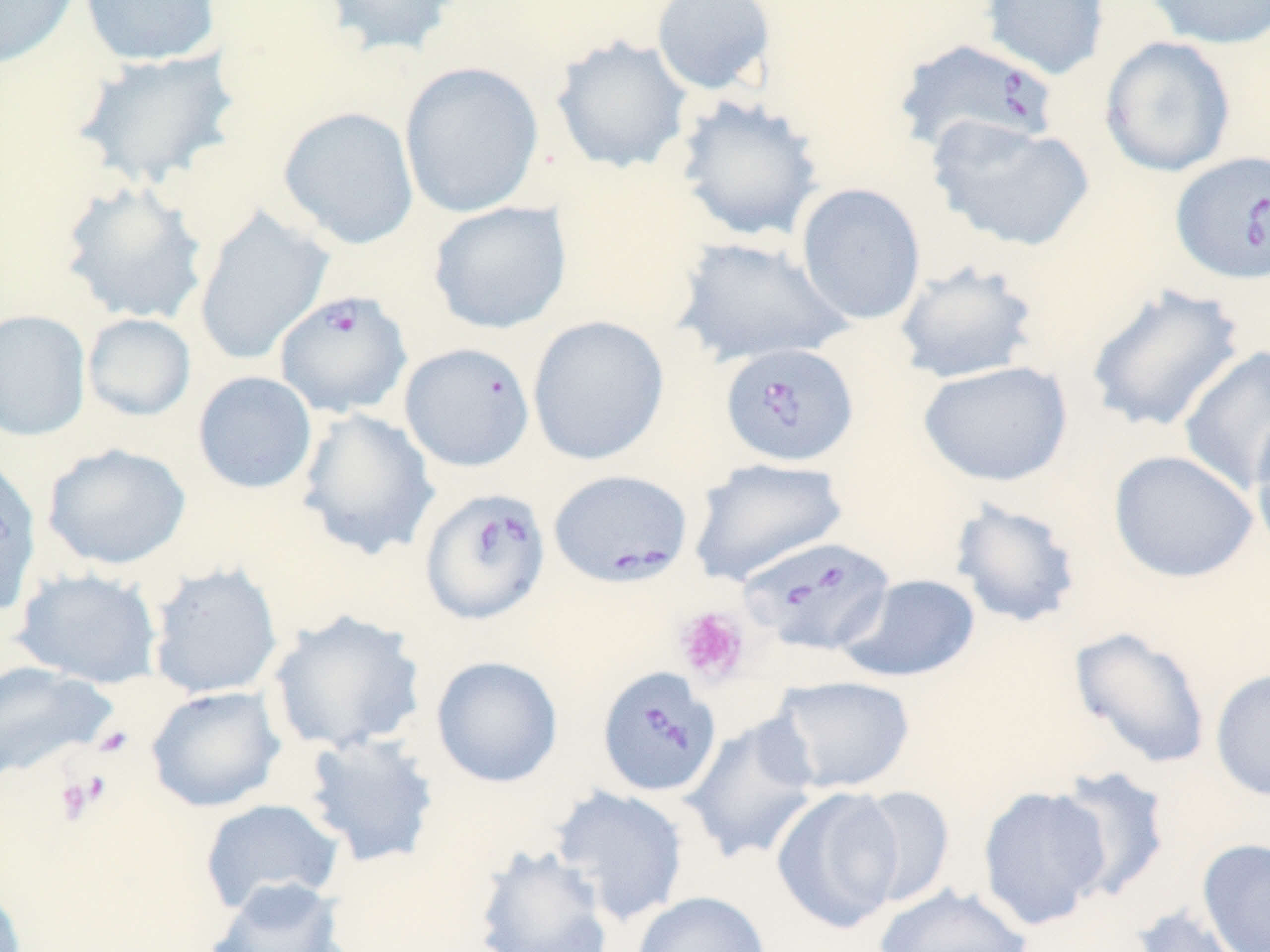
Approximate bounding boxes as [x1, y1, x2, y2] in pixels. Babesia divergens-infected red blood cell locations: [891, 38, 1061, 157], [1170, 150, 1270, 285], [273, 290, 414, 418], [719, 342, 860, 467], [548, 468, 694, 588], [419, 486, 553, 626], [740, 537, 897, 659], [597, 666, 722, 798]. Platelet locations: [673, 605, 751, 686], [92, 725, 134, 758], [53, 775, 102, 824]. Uninfected red blood cell locations: [0, 0, 81, 70], [78, 0, 222, 67], [322, 0, 465, 58], [650, 0, 778, 97], [980, 0, 1110, 82], [1143, 0, 1270, 50], [550, 35, 694, 175], [1099, 36, 1237, 178], [70, 46, 243, 190], [399, 61, 544, 218], [674, 94, 824, 244], [277, 106, 420, 250], [927, 117, 1096, 253], [58, 178, 210, 327], [795, 182, 927, 326], [427, 201, 572, 334], [192, 207, 333, 366], [671, 235, 853, 369], [893, 258, 1041, 385], [1084, 283, 1246, 434], [0, 308, 92, 442], [82, 313, 197, 422], [526, 315, 670, 467], [399, 342, 535, 472], [1177, 345, 1270, 495], [918, 360, 1073, 487], [192, 370, 318, 495], [295, 407, 439, 561], [1248, 411, 1270, 562], [42, 443, 191, 571], [1108, 449, 1259, 584], [0, 456, 41, 618], [686, 456, 849, 586], [948, 498, 1083, 629], [147, 562, 284, 699], [12, 568, 163, 688], [837, 573, 981, 683], [266, 608, 427, 756], [1069, 626, 1212, 770], [430, 655, 564, 788], [0, 661, 118, 782], [1209, 667, 1270, 802], [769, 675, 917, 793], [144, 685, 286, 813], [681, 712, 823, 866], [299, 731, 442, 869], [1051, 766, 1172, 903], [549, 784, 691, 926], [977, 785, 1113, 931], [849, 786, 956, 909], [771, 787, 906, 934], [199, 797, 345, 917], [1197, 838, 1270, 952], [472, 844, 614, 952], [203, 877, 350, 952], [0, 880, 27, 952], [873, 883, 1032, 952], [631, 891, 772, 952], [1129, 904, 1250, 952]. Slide-level diagnosis: Babesia divergens. Image is 1270×952 pixels. One field of a larger specimen. May-Grünwald-Giemsa stain. Thin blood film. Optical microscopy. Captured at 1000x magnification.